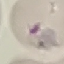
Summary:
  - Malaria status: uninfected
  - Capture: smartphone camera at the microscope eyepiece
  - Image type: cell patch, automatically extracted from a larger field of view and resized to 64 × 64 pixels
  - Stain: Giemsa
  - Preparation: thin smear